Name the parasite shown.
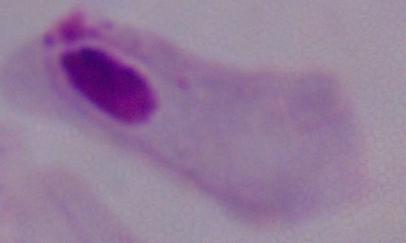
A trichomonad.

modality = photomicrograph
magnification = 1000x